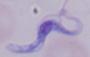
Captured at 1000x magnification. Micrograph. A trypanosome is seen.